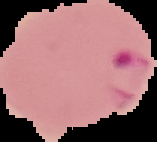
preparation = thin blood film
result = malaria parasites identified
image type = segmented cell region with the area outside set to black
image size = 157×142 pixels